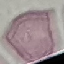 Result: no malaria parasites seen. Thin blood film. Photographed with a smartphone camera at the microscope eyepiece. Giemsa stain. Automatically extracted cell patch, resized to 64 × 64 pixels.